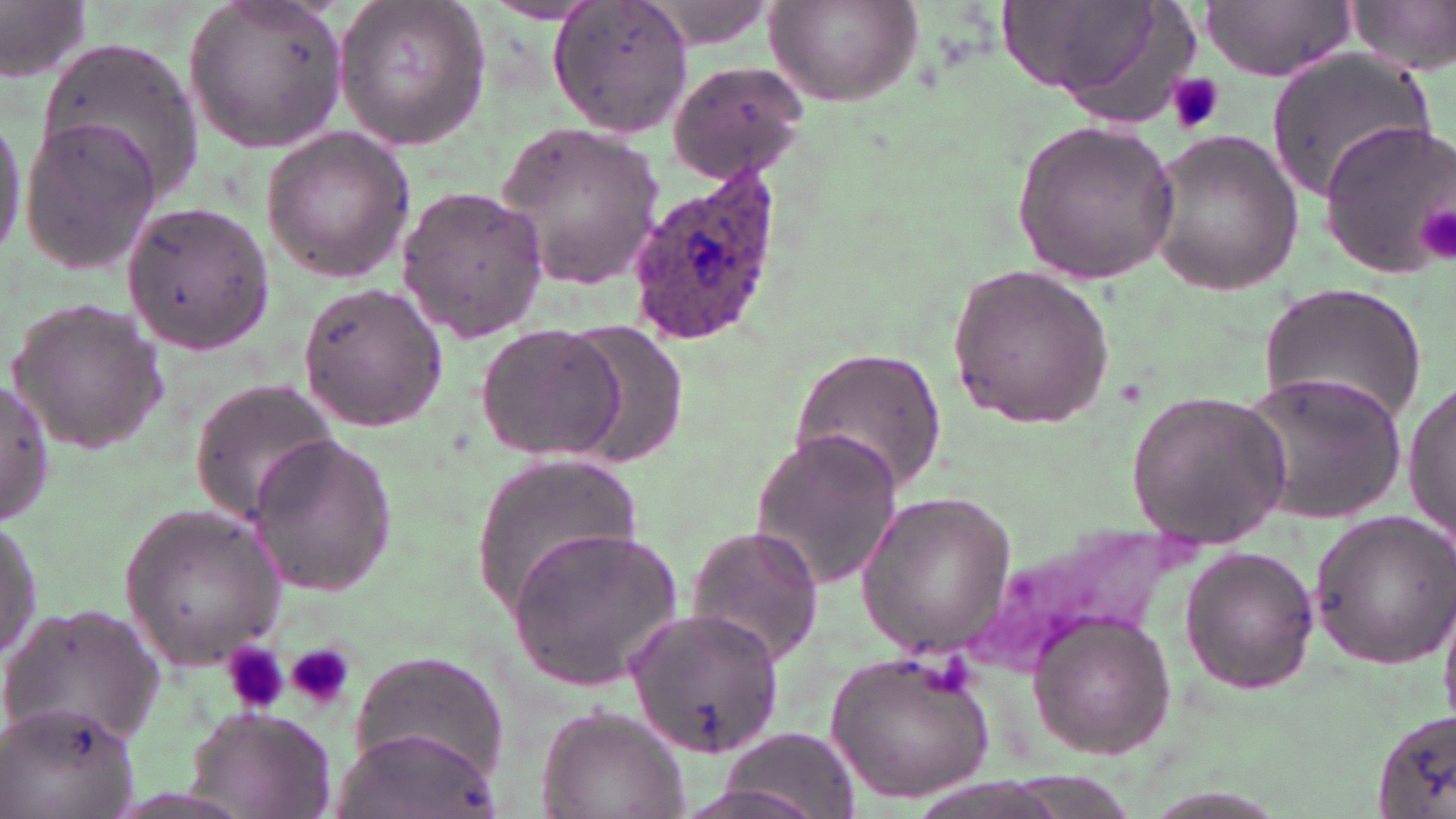
Summary:
  - Coordinate format: approximate bounding boxes as (x1,y1)-(x2,y2) corner pairs in pixels
  - Platelet locations: (1164,72)-(1226,135), (1420,198)-(1455,265), (222,641)-(288,715), (238,642)-(335,716), (287,642)-(355,709)
  - Uninfected red blood cell locations: (0,0)-(91,83), (184,0)-(346,152), (333,0)-(490,152), (550,0)-(696,139), (763,0)-(925,110), (1006,0)-(1196,125), (1345,0)-(1456,76), (629,1)-(788,52), (1201,1)-(1356,80), (35,40)-(204,201), (1260,48)-(1440,202), (663,60)-(808,185), (0,106)-(28,269), (19,114)-(159,272), (1320,118)-(1455,277), (1012,119)-(1181,283), (494,122)-(667,290), (259,127)-(414,280), (1143,131)-(1304,296), (394,182)-(552,342), (120,199)-(274,357), (946,264)-(1116,428), (1260,281)-(1429,425), (296,282)-(448,431), (6,296)-(167,457), (476,320)-(625,464), (566,321)-(689,469), (789,346)-(948,498), (1238,369)-(1410,528), (188,379)-(343,524), (1405,379)-(1456,551), (0,381)-(55,526), (1125,391)-(1293,546), (748,428)-(903,592), (241,432)-(399,595), (468,454)-(645,617), (856,492)-(1017,655), (119,505)-(285,667), (1310,508)-(1456,671), (0,514)-(43,670), (973,518)-(1196,681), (682,524)-(827,669), (506,527)-(682,690), (1179,544)-(1320,694), (2,600)-(165,750), (625,606)-(783,759), (1029,612)-(1176,757), (349,649)-(508,787), (825,650)-(995,807), (5,699)-(137,819), (186,703)-(335,819), (536,707)-(687,819), (1373,709)-(1456,819), (334,722)-(498,819), (710,726)-(861,817)
  - Plasmodium ovale-infected red blood cell locations: (626,164)-(786,344)
  - Slide-level diagnosis: Plasmodium ovale
  - Magnification: 1000x
  - Preparation: thin blood film
  - Image size: 1456×819 pixels
  - Field of view: one of a larger specimen
  - Stain: May-Grünwald-Giemsa
  - Modality: optical microscopy